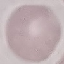
Result: no malaria parasites seen. Acquired by smartphone through the microscope eyepiece. Automatically extracted cell patch, resized to 64 × 64 pixels. Thin blood film. Giemsa stain.